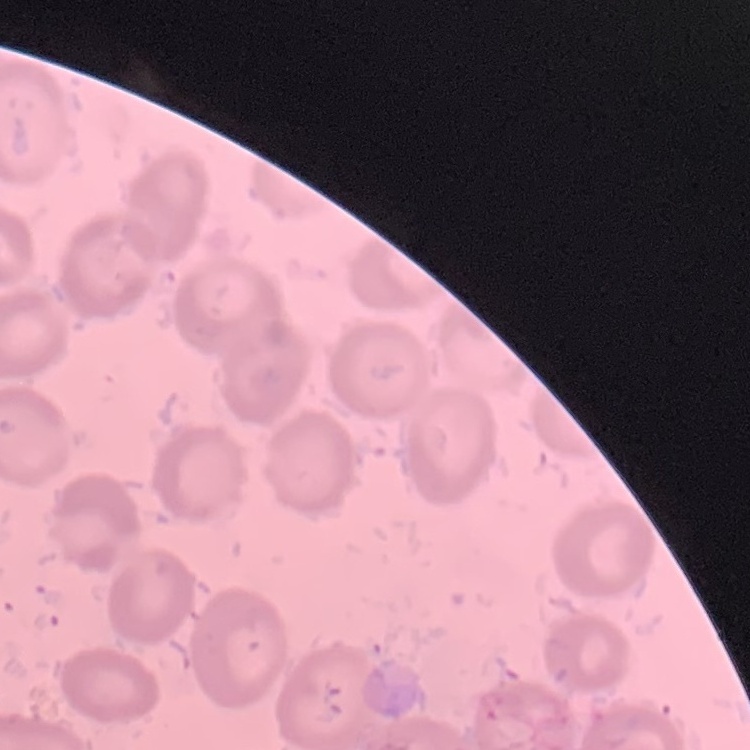

Summary:
  - Erythrocyte morphology: no rouleaux formation
  - Preparation: thin blood film
  - Stain: Field's or Giemsa
  - Image type: square crop of a larger photomicrograph